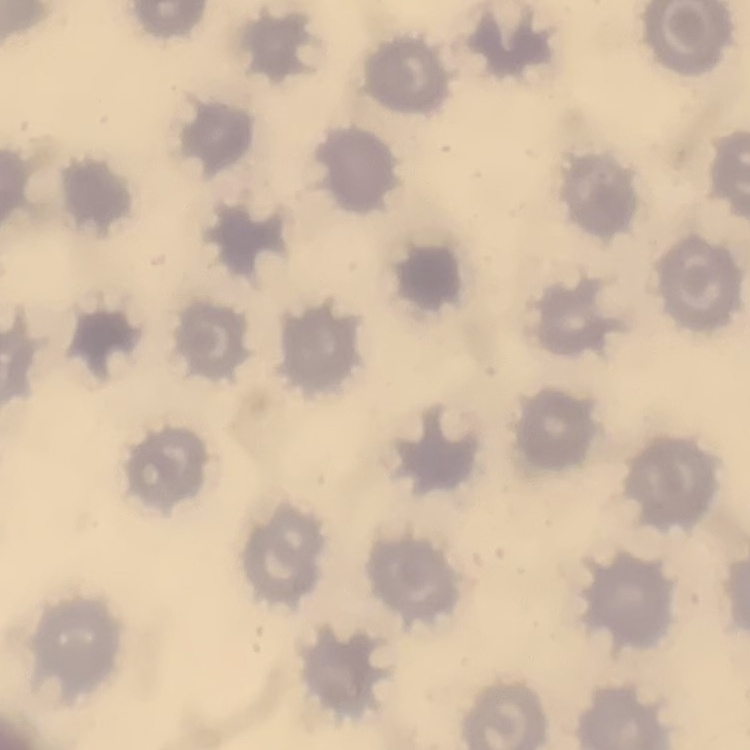 The erythrocytes exhibit no rouleaux formation. One tile cut from a larger photomicrograph. Thin peripheral smear. Stained with either Field's or Giemsa.